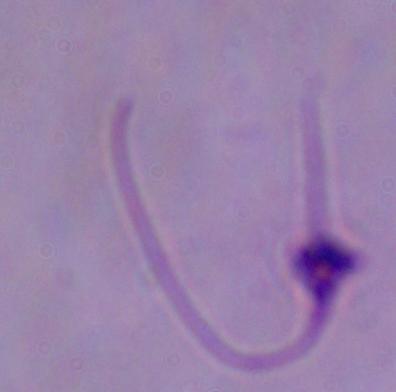
Summary:
  - Identification: Leishmania
  - Modality: micrograph
  - Magnification: 1000x